Name the parasite shown.
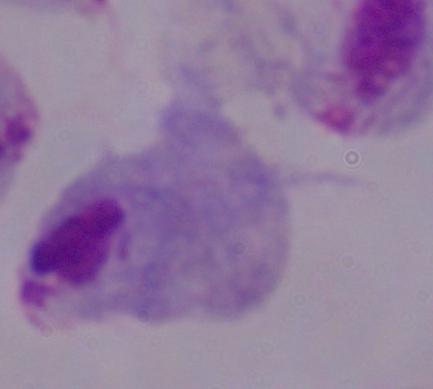

This is a trichomonad.

Captured at 1000x magnification. Micrograph.